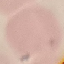

Summary:
  - Result: no malaria parasites detected
  - Image type: cell patch, automatically extracted from a larger field of view and resized to 64 × 64 pixels
  - Capture: smartphone camera at the microscope eyepiece
  - Stain: Giemsa
  - Preparation: thin smear